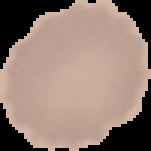
Summary:
  - Preparation: thin blood smear
  - Image type: cell region segmented out of the field of view; surrounding area masked to black
  - Image size: 151×151 pixels
  - Malaria status: uninfected